Report the malaria status of this cell.
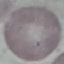

It is uninfected.

Thin blood film. Giemsa-stained preparation. Photographed with a smartphone camera at the microscope eyepiece. Cell patch, automatically extracted from a larger field of view and resized to 64 × 64 pixels.